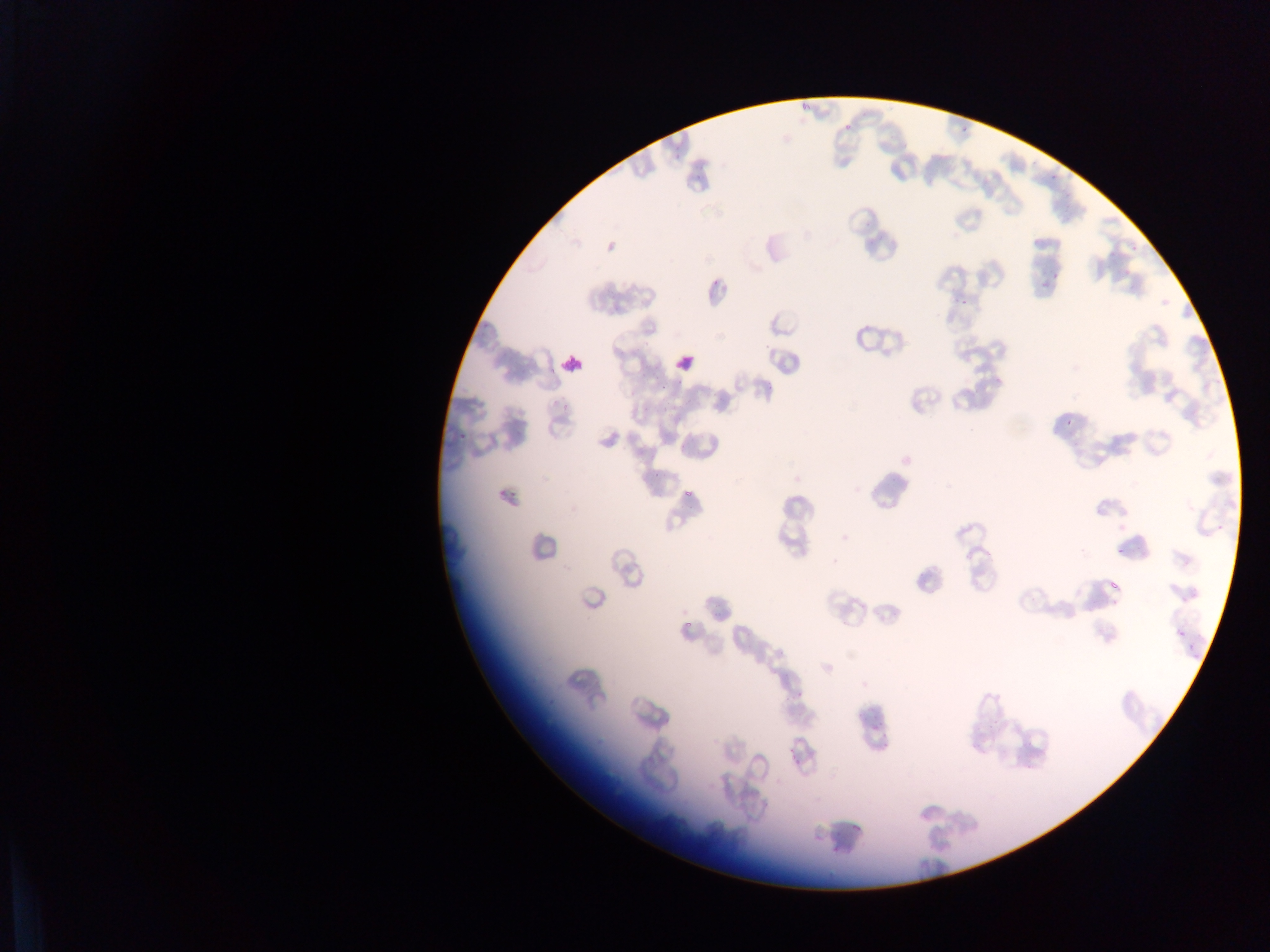
Approximate bounding boxes as (left, top, right, bottom) in pixels. Leukocyte locations: (554, 347, 590, 383), (669, 347, 702, 380). Plasmodium parasite locations: (842, 121, 854, 134), (960, 126, 976, 135), (1046, 175, 1062, 185), (1042, 272, 1061, 286), (956, 295, 974, 306), (1061, 416, 1079, 427), (683, 486, 697, 501). Collected in Ghana. Photographed through a microscope with a mobile-phone camera. Image is 1270×952 pixels. Thin blood smear. One field of view.